Give the preparation type.
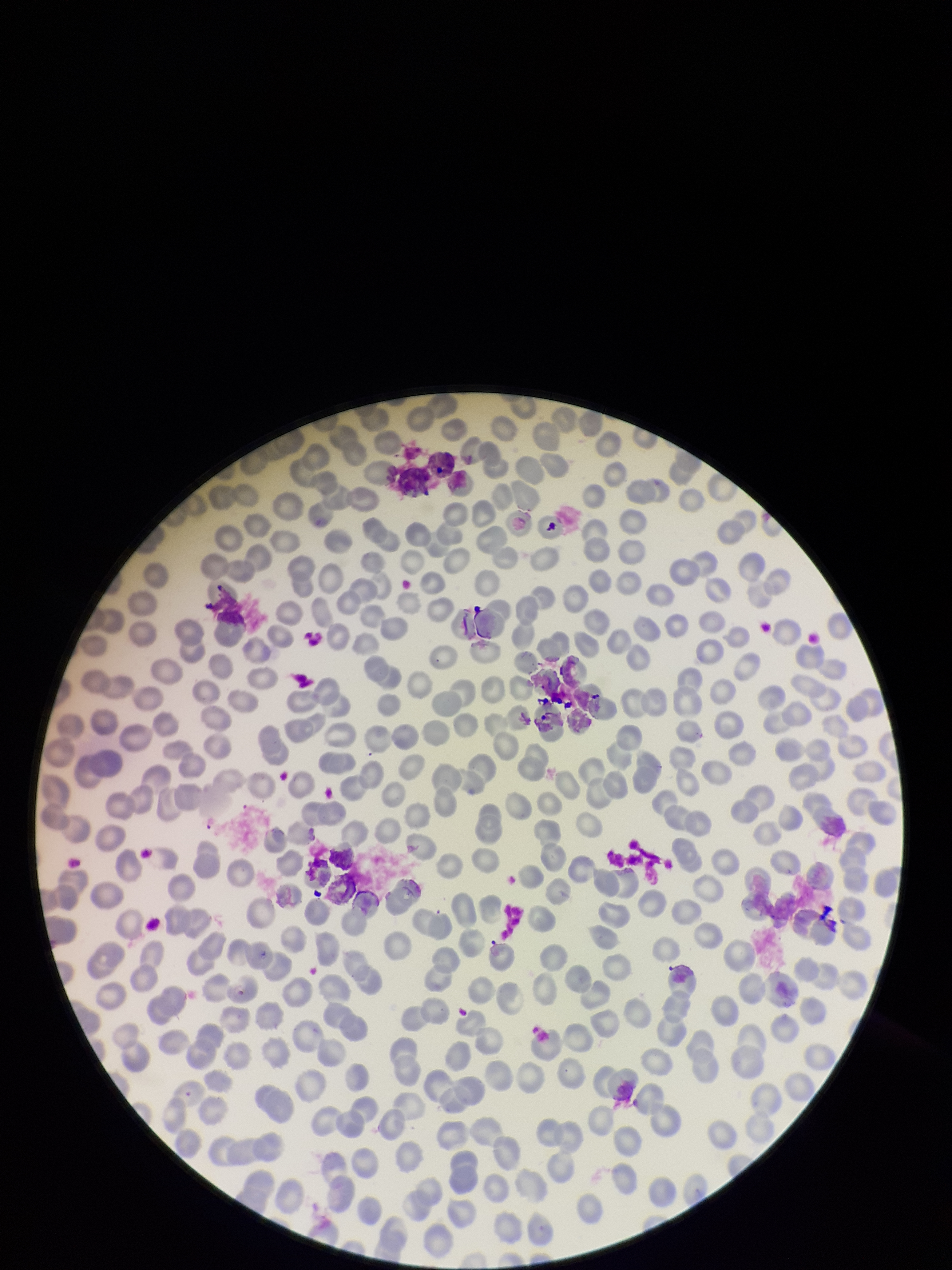
A thin smear.

Summary:
  - Red blood cell count: 295
  - Patient malaria status: negative
  - Parasitized red blood cells: none identified
  - Image size: 952×1270 pixels
  - Parasitized red blood cell count: 0
  - Stain: Giemsa
  - Field of view: single
  - Capture: smartphone photograph through the microscope eyepiece